Classify this cell by malaria status.
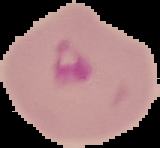
Parasitized.

image size = 160×148 pixels
image type = segmented cell region on a black background
preparation = thin blood smear